Assess the morphology of the red blood cells.
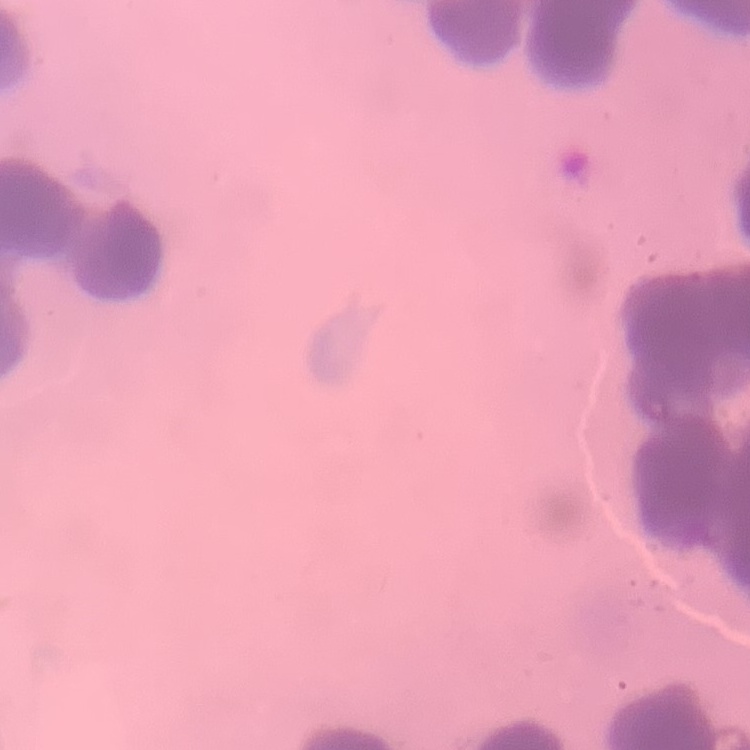
They show rouleaux formation.

image type = one tile cut from a larger photomicrograph
preparation = thin peripheral smear
stain = Field's or Giemsa